Find each white blood cell.
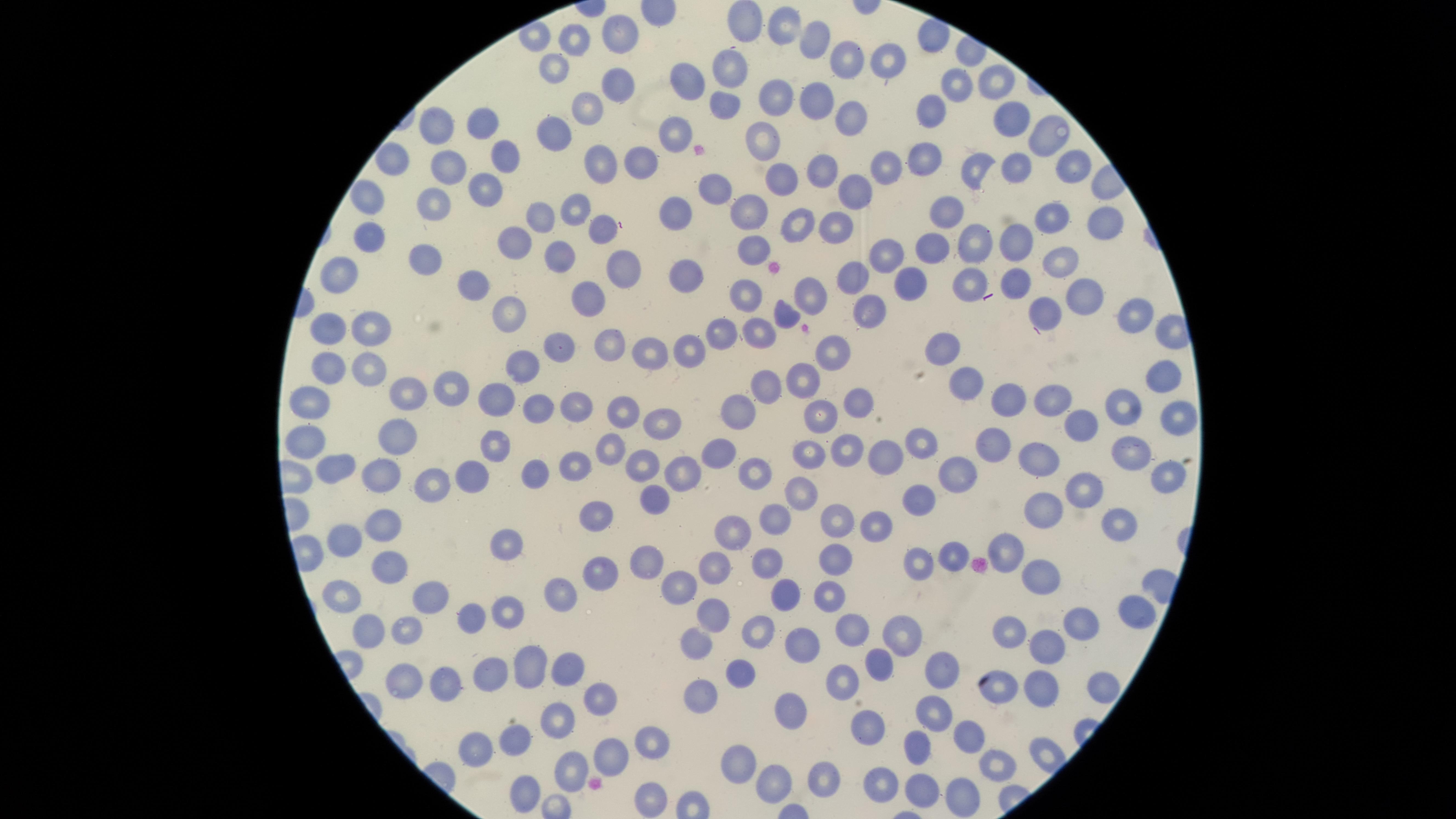

No white blood cells identified.

Approximate marker points as (x, y) in pixels.
Summary:
  - Uninfected red blood cells: (745, 22), (789, 25), (820, 35), (617, 38), (572, 41), (845, 60), (890, 62), (730, 65), (554, 66), (995, 81), (617, 84), (956, 89), (693, 90), (816, 97), (776, 98), (585, 109), (722, 110), (927, 111), (854, 112), (1006, 118), (482, 123), (559, 129), (435, 131), (680, 131), (1043, 135), (763, 138), (501, 155), (919, 157), (889, 159), (390, 161), (1070, 163), (638, 164), (1021, 166), (599, 169), (450, 171), (821, 171), (976, 171), (779, 181), (856, 186), (716, 189), (482, 190), (364, 198), (436, 204), (578, 212), (678, 212), (751, 213), (540, 215), (943, 216), (1051, 219), (800, 222), (1101, 224), (597, 226), (841, 228), (518, 236), (368, 237), (975, 239), (1021, 243), (933, 245), (752, 252), (885, 254), (428, 255), (558, 257), (622, 260), (1063, 260), (689, 268), (857, 276), (339, 277), (913, 282), (474, 283), (968, 284), (809, 290), (741, 291), (1082, 291), (584, 294), (1045, 309), (511, 311), (872, 313), (1133, 314), (784, 315), (374, 326), (330, 327), (763, 333), (721, 334), (607, 344), (946, 345), (560, 346), (692, 348), (654, 352), (830, 352), (330, 362), (524, 368), (370, 369), (1164, 379), (964, 381), (806, 383), (450, 384), (764, 388), (404, 392), (500, 396), (1052, 398), (308, 400), (1019, 400), (854, 401), (566, 402), (1120, 405), (537, 408), (822, 410), (741, 411), (619, 412), (1171, 412), (1088, 421), (659, 422), (394, 435), (303, 438), (494, 442), (922, 442), (1002, 444), (850, 445), (607, 446), (720, 452), (810, 454), (1131, 454), (1039, 456), (889, 457), (572, 464), (641, 464), (330, 467), (761, 471), (535, 472), (682, 472), (958, 472), (376, 475), (1164, 475), (471, 476), (429, 484), (1084, 485), (802, 487), (648, 498), (915, 500), (1039, 510), (775, 518), (592, 519), (835, 519), (1117, 522), (877, 523), (377, 526), (735, 529), (505, 539), (343, 542), (1009, 551), (836, 554), (950, 554), (641, 559), (764, 559), (916, 563), (715, 566), (386, 567), (597, 574), (1037, 577), (676, 584), (340, 587), (783, 591), (830, 593), (428, 595), (560, 595), (1136, 608), (710, 612), (502, 614), (465, 615), (1074, 626), (400, 630), (852, 630), (365, 632), (1010, 632), (758, 633), (895, 638), (804, 643), (696, 644), (1045, 648), (878, 660), (943, 662), (527, 667), (568, 667), (738, 668), (490, 672), (441, 683), (402, 684), (847, 685), (1039, 686), (1103, 686), (996, 688), (701, 698), (602, 702), (789, 705), (936, 712), (558, 722), (869, 729), (964, 736), (513, 740), (650, 744), (474, 749), (915, 751), (603, 754), (740, 758), (1000, 763), (569, 772), (818, 773), (879, 776), (769, 778), (923, 787), (960, 791), (649, 792), (520, 794)
  - Capture: smartphone photograph through the microscope eyepiece
  - Visible region: circular
  - Stain: Giemsa
  - Preparation: thin blood smear
  - Field of view: single
  - Image size: 1456×819 pixels
  - Presence: no malaria parasites identified